Report the malaria status of this cell.
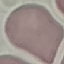
Uninfected.

stain = Giemsa
preparation = thin blood smear
capture = smartphone through the microscope eyepiece
image type = automatically extracted cell patch, resized to 64 × 64 pixels